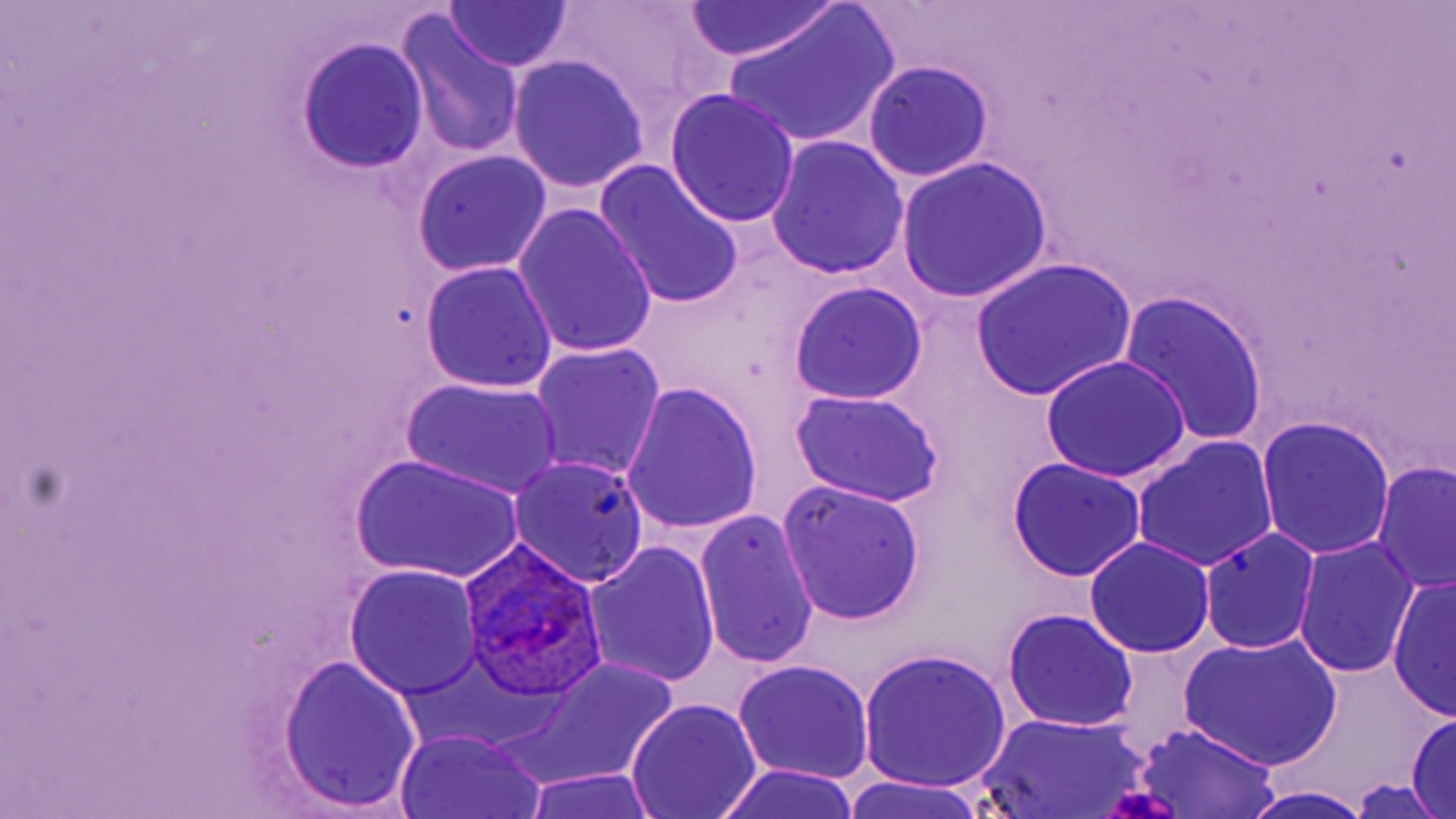

Summary:
  - Coordinate format: approximate bounding boxes as named x1/y1/x2/y2 corners in pixels
  - Plasmodium ovale-infected red blood cell locations: (x1=461, y1=538, x2=607, y2=703)
  - Uninfected red blood cell locations: (x1=444, y1=1, x2=573, y2=73), (x1=545, y1=1, x2=721, y2=123), (x1=682, y1=2, x2=841, y2=63), (x1=721, y1=5, x2=899, y2=150), (x1=399, y1=15, x2=524, y2=160), (x1=297, y1=39, x2=429, y2=173), (x1=508, y1=55, x2=649, y2=194), (x1=864, y1=61, x2=994, y2=182), (x1=665, y1=91, x2=802, y2=229), (x1=767, y1=136, x2=910, y2=280), (x1=411, y1=149, x2=552, y2=276), (x1=896, y1=157, x2=1053, y2=304), (x1=594, y1=163, x2=746, y2=311), (x1=514, y1=203, x2=658, y2=361), (x1=969, y1=258, x2=1137, y2=400), (x1=420, y1=261, x2=558, y2=394), (x1=791, y1=281, x2=928, y2=406), (x1=1120, y1=294, x2=1271, y2=448), (x1=531, y1=343, x2=665, y2=480), (x1=1039, y1=355, x2=1193, y2=481), (x1=402, y1=377, x2=564, y2=498), (x1=621, y1=381, x2=764, y2=537), (x1=789, y1=389, x2=945, y2=509), (x1=1256, y1=416, x2=1395, y2=561), (x1=1132, y1=438, x2=1278, y2=572), (x1=350, y1=453, x2=523, y2=582), (x1=508, y1=456, x2=649, y2=588), (x1=1006, y1=457, x2=1146, y2=581), (x1=1373, y1=462, x2=1455, y2=594), (x1=777, y1=480, x2=926, y2=626), (x1=693, y1=509, x2=819, y2=671), (x1=1199, y1=528, x2=1321, y2=654), (x1=1085, y1=536, x2=1215, y2=658), (x1=1294, y1=538, x2=1420, y2=677), (x1=584, y1=541, x2=722, y2=689), (x1=343, y1=566, x2=483, y2=699), (x1=1387, y1=577, x2=1455, y2=722), (x1=1002, y1=609, x2=1139, y2=733), (x1=1179, y1=635, x2=1342, y2=771), (x1=859, y1=648, x2=1013, y2=796), (x1=278, y1=656, x2=420, y2=815), (x1=490, y1=657, x2=683, y2=790), (x1=734, y1=660, x2=875, y2=784), (x1=627, y1=699, x2=761, y2=818), (x1=978, y1=711, x2=1154, y2=819), (x1=1408, y1=714, x2=1455, y2=819), (x1=1130, y1=723, x2=1285, y2=819), (x1=395, y1=732, x2=542, y2=819), (x1=709, y1=764, x2=866, y2=819), (x1=518, y1=771, x2=666, y2=819), (x1=842, y1=777, x2=996, y2=818), (x1=1346, y1=777, x2=1444, y2=818), (x1=1244, y1=787, x2=1374, y2=819)
  - Slide-level diagnosis: Plasmodium ovale
  - Field of view: single
  - Image size: 1456×819 pixels
  - Magnification: 1000x
  - Modality: optical microscopy
  - Stain: May-Grünwald-Giemsa
  - Preparation: thin blood smear